Name the parasite shown.
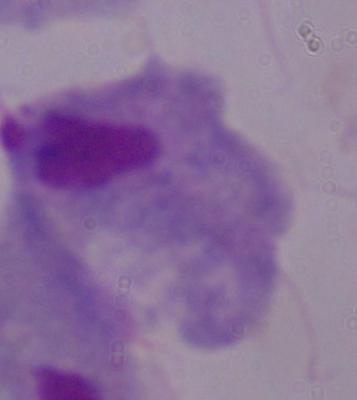

A trichomonad.

1000x magnification. Photomicrograph.